Report the malaria status of this cell.
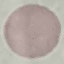
It is uninfected.

Photographed with a smartphone camera at the microscope eyepiece. Thin blood smear. Giemsa-stained preparation. Cell patch, automatically extracted from a larger field of view and resized to 64 × 64 pixels.